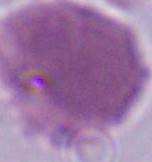

Summary:
  - Identification: erythrocyte
  - Magnification: 1000x
  - Modality: micrograph